Locate every Plasmodium falciparum-infected red blood cell.
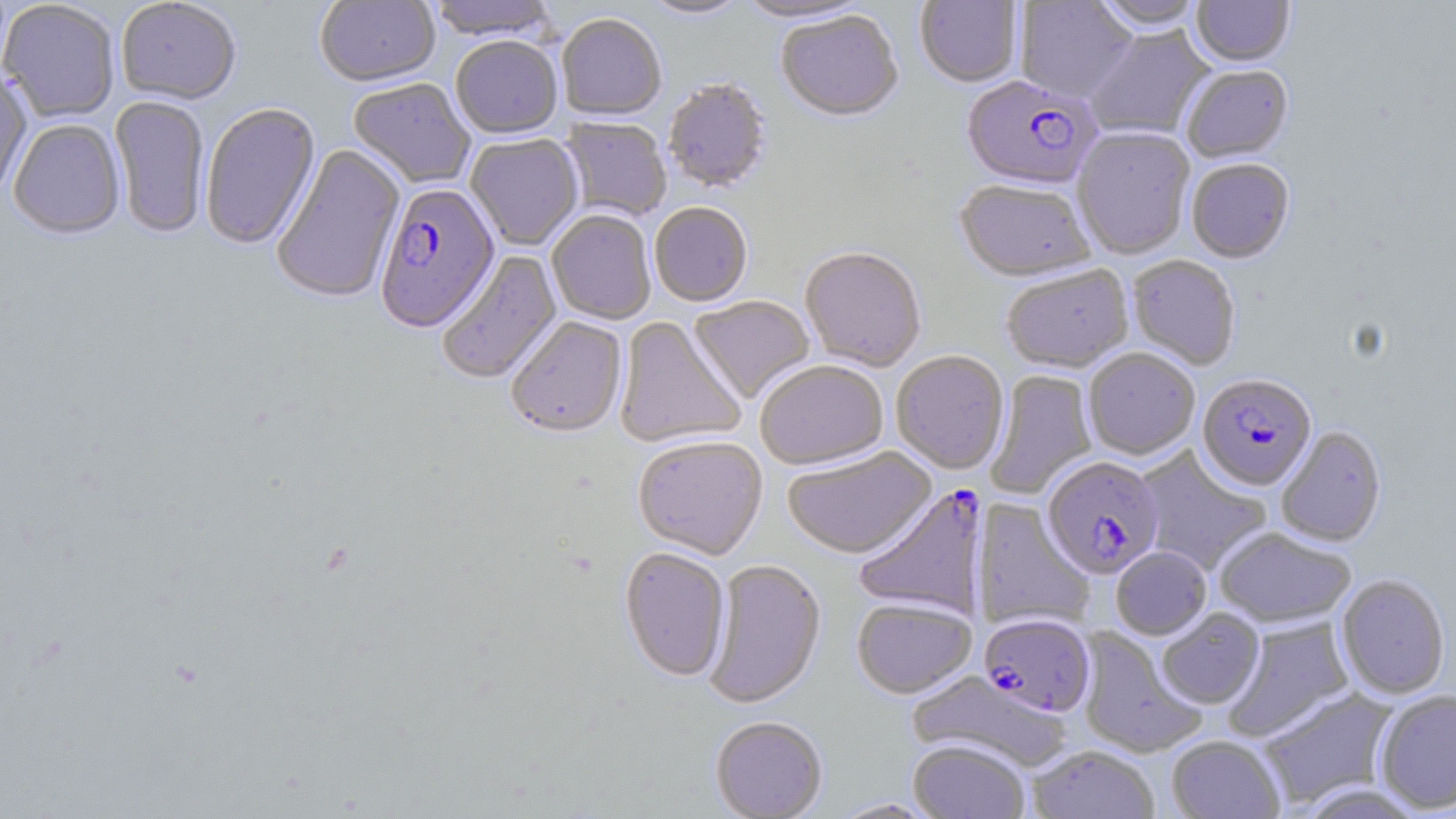
Approximate bounding boxes as [x1, y1, x2, y2] in pixels.
Plasmodium falciparum-infected red blood cells: [961, 77, 1102, 193], [375, 183, 500, 334], [1198, 374, 1316, 493], [1042, 457, 1164, 580], [854, 484, 989, 622], [980, 614, 1097, 718].

slide-level diagnosis = Plasmodium falciparum
magnification = 1000x
image size = 1456×819 pixels
stain = May-Grünwald-Giemsa
preparation = thin blood smear
uninfected red blood cell locations = approximate bounding boxes as [x1, y1, x2, y2] in pixels: [116, 0, 242, 105], [314, 0, 440, 89], [427, 0, 558, 43], [640, 0, 751, 21], [733, 0, 875, 25], [1092, 0, 1206, 33], [1191, 0, 1294, 69], [914, 1, 1023, 89], [1014, 1, 1138, 104], [0, 2, 121, 123], [776, 13, 902, 125], [556, 16, 666, 123], [1084, 26, 1214, 140], [450, 37, 563, 140], [1181, 67, 1294, 164], [0, 69, 33, 200], [348, 79, 476, 189], [662, 79, 773, 194], [109, 96, 210, 239], [201, 103, 321, 250], [560, 117, 671, 222], [9, 120, 125, 240], [1073, 129, 1195, 261], [465, 134, 583, 251], [270, 143, 406, 305], [1186, 160, 1295, 265], [953, 181, 1096, 284], [650, 204, 752, 307], [546, 210, 656, 325], [799, 248, 927, 372], [436, 249, 562, 386], [1127, 255, 1241, 371], [1001, 265, 1134, 374], [688, 295, 816, 405], [505, 317, 627, 440], [614, 317, 746, 449], [1083, 349, 1200, 460], [891, 351, 1009, 476], [755, 361, 889, 471], [985, 370, 1098, 499], [1275, 426, 1387, 548], [633, 436, 768, 561], [1135, 445, 1272, 577], [782, 447, 936, 561], [972, 498, 1094, 632], [1215, 527, 1357, 630], [1111, 547, 1211, 640], [619, 548, 731, 683], [703, 558, 826, 710], [1336, 574, 1450, 700], [852, 598, 977, 699], [1156, 608, 1265, 710], [1221, 616, 1355, 742], [1076, 626, 1207, 758], [907, 671, 1073, 773], [1257, 687, 1399, 809], [1374, 690, 1456, 814], [710, 717, 828, 819], [1167, 736, 1285, 819], [908, 740, 1030, 819], [1028, 745, 1159, 819], [1295, 783, 1428, 819], [830, 798, 939, 818]
modality = light microscopy
field of view = single